Mark where platelets are.
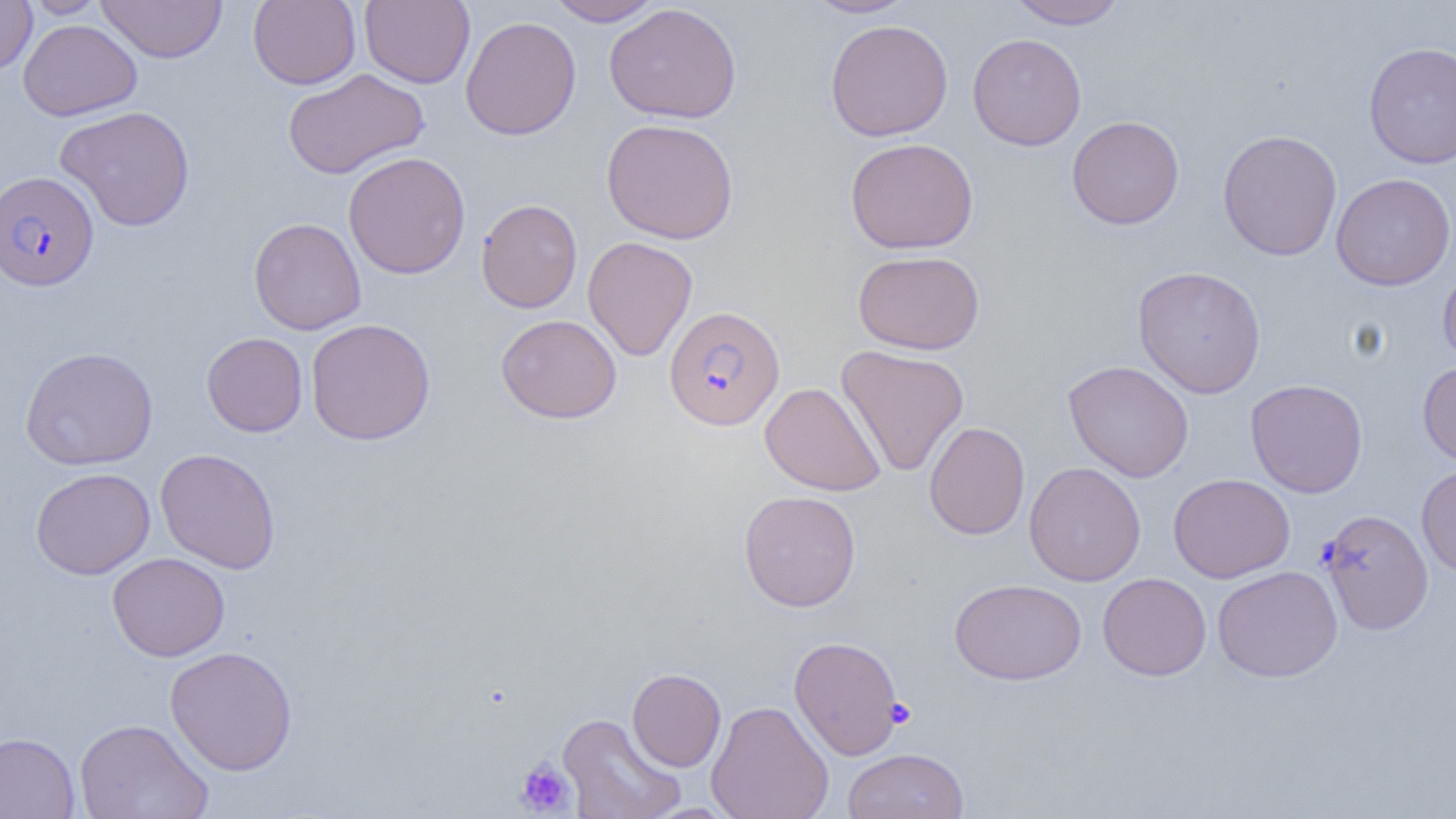

Approximate bounding boxes as [x1, y1, x2, y2] in pixels.
Platelets: [885, 698, 916, 728], [516, 759, 575, 815].

slide-level diagnosis = Plasmodium falciparum
image size = 1456×819 pixels
magnification = 1000x
modality = optical microscopy
preparation = thin blood smear
Plasmodium falciparum-infected red blood cell locations = approximate bounding boxes as [x1, y1, x2, y2] in pixels: [0, 170, 98, 291], [664, 305, 785, 431], [1318, 509, 1433, 634]
field of view = single
uninfected red blood cell locations = approximate bounding boxes as [x1, y1, x2, y2] in pixels: [0, 0, 37, 74], [23, 0, 111, 18], [96, 0, 228, 63], [248, 0, 361, 89], [359, 0, 475, 88], [546, 0, 664, 26], [803, 0, 917, 19], [1006, 1, 1129, 29], [604, 2, 742, 124], [460, 16, 581, 140], [18, 18, 143, 121], [825, 18, 953, 142], [967, 32, 1087, 151], [1363, 41, 1456, 169], [282, 69, 430, 180], [55, 105, 195, 232], [1067, 115, 1184, 229], [601, 118, 739, 244], [1217, 129, 1343, 261], [845, 137, 978, 254], [343, 151, 471, 279], [1331, 173, 1456, 291], [476, 198, 583, 313], [248, 217, 366, 334], [583, 236, 697, 361], [852, 250, 985, 355], [1438, 262, 1456, 372], [1132, 265, 1266, 398], [496, 314, 622, 424], [306, 318, 436, 446], [202, 332, 308, 437], [835, 344, 969, 477], [20, 346, 158, 470], [1063, 360, 1194, 482], [1417, 361, 1456, 469], [1245, 379, 1368, 497], [760, 381, 885, 497], [924, 422, 1030, 540], [155, 448, 281, 574], [1024, 461, 1146, 586], [1416, 463, 1456, 578], [30, 467, 156, 579], [1168, 473, 1296, 583], [738, 490, 861, 612], [107, 552, 230, 661], [1212, 565, 1342, 682], [1097, 572, 1212, 681], [949, 578, 1086, 685], [788, 635, 904, 760], [164, 645, 298, 776], [627, 668, 726, 772], [706, 700, 834, 819], [557, 712, 686, 819], [73, 717, 213, 819], [0, 731, 79, 819], [842, 747, 969, 819]